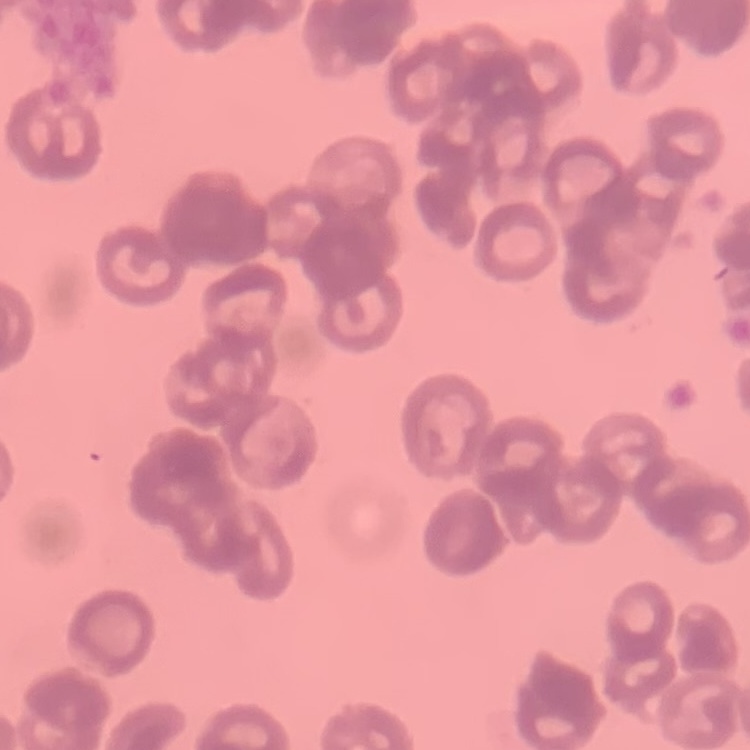 The erythrocytes show rouleaux formation. Thin blood film. Field's or Giemsa stain. Square crop of a larger photomicrograph.